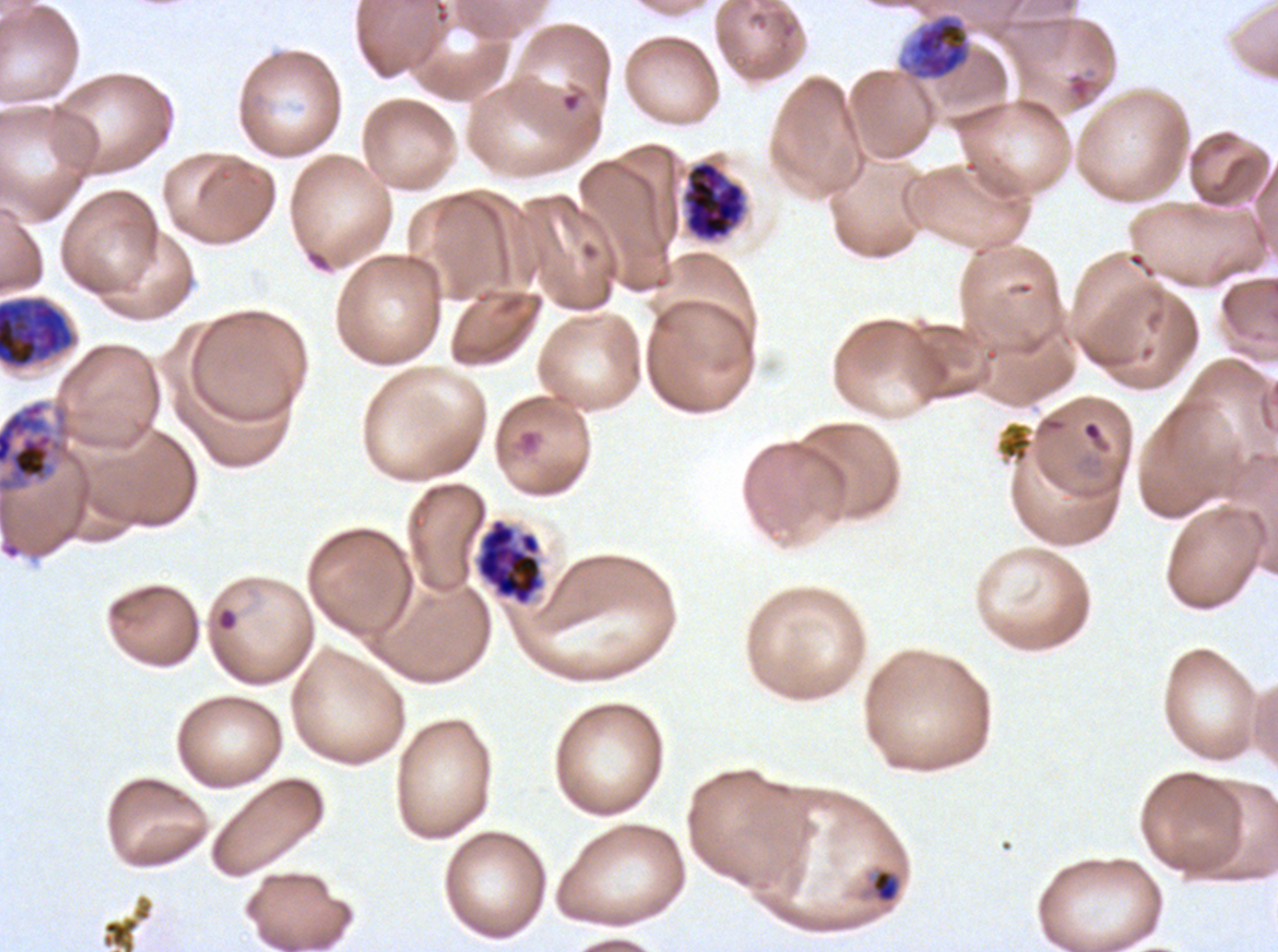
notation = approximate bounding boxes as {x1, y1, x2, y2} in pixels
late schizont locations = {682, 160, 746, 241}
late-ring/early-trophozoite locations = {871, 870, 898, 902}
ring locations = {559, 87, 586, 114}, {215, 606, 239, 632}
early schizont locations = {0, 298, 74, 368}, {0, 400, 63, 493}
late trophozoite locations = {897, 13, 972, 81}
segmenter locations = {474, 518, 546, 606}
stain = Giemsa
preparation = thin blood film
specimen = Plasmodium falciparum cultured ex vivo for 24 to 48 hours, from a patient in The Gambia
life-cycle stages observed = ring, late-ring/early-trophozoite, late trophozoite, early schizont, late schizont, segmenter
field of view = sub-image separated from a larger composite
image size = 1278×952 pixels